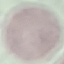

Result: no malaria parasites detected. Acquired by smartphone through the microscope eyepiece. Giemsa-stained preparation. Thin blood film. Automatically extracted cell patch, resized to 64 × 64 pixels.